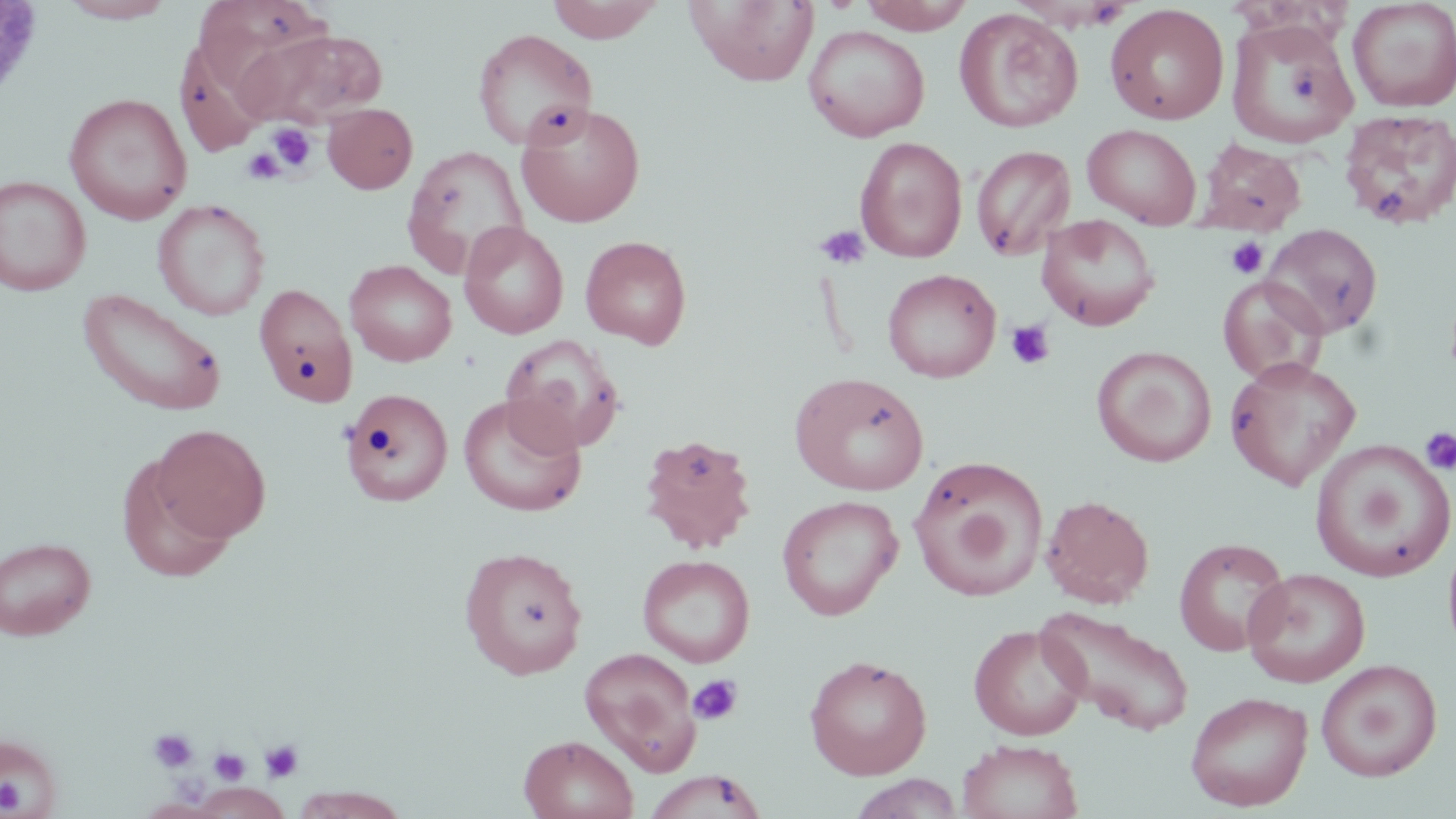

Summary:
  - Coordinate format: approximate bounding boxes as (x1,y1)-(x2,y2) corner pairs in pixels
  - Uninfected red blood cell locations: (59,0)-(176,23), (194,0)-(329,90), (546,0)-(665,43), (686,0)-(819,86), (856,0)-(976,33), (1347,0)-(1456,113), (1105,4)-(1229,125), (954,8)-(1083,133), (1226,17)-(1359,150), (803,25)-(930,142), (234,28)-(388,128), (472,29)-(597,150), (175,39)-(270,156), (64,92)-(193,225), (516,102)-(645,227), (323,103)-(418,194), (1338,108)-(1456,230), (1082,124)-(1201,227), (854,136)-(968,263), (1197,139)-(1307,233), (401,144)-(530,278), (970,144)-(1076,261), (0,175)-(92,296), (153,199)-(270,321), (1036,214)-(1160,331), (459,222)-(569,339), (1262,223)-(1383,338), (580,235)-(692,349), (345,259)-(457,367), (882,268)-(1001,382), (1218,275)-(1329,386), (253,283)-(358,407), (77,288)-(228,417), (500,334)-(625,454), (1092,346)-(1217,467), (1225,356)-(1361,490), (789,371)-(930,496), (340,387)-(455,507), (458,395)-(586,518), (152,424)-(270,543), (638,433)-(758,554), (1310,438)-(1456,582), (116,454)-(239,581), (908,455)-(1048,602), (1041,494)-(1155,608), (776,495)-(903,620), (0,536)-(96,640), (1173,537)-(1291,657), (458,545)-(588,680), (637,554)-(755,667), (1244,567)-(1371,688), (1036,606)-(1196,736), (968,624)-(1089,741), (579,646)-(702,774), (804,654)-(932,779), (1316,659)-(1443,781), (1185,690)-(1313,811), (0,731)-(64,816), (519,734)-(639,819), (957,739)-(1084,819), (642,770)-(768,819), (850,773)-(963,818), (193,783)-(290,817), (289,787)-(411,818), (139,799)-(221,818)
  - Platelet locations: (267,123)-(317,173), (242,147)-(285,185), (814,224)-(871,270), (1225,235)-(1269,279), (1006,320)-(1055,370), (1419,427)-(1456,475), (688,674)-(744,726), (148,727)-(198,773), (259,738)-(305,783), (209,747)-(250,786), (0,776)-(25,814)
  - Slide-level diagnosis: negative for blood parasites
  - Stain: May-Grünwald-Giemsa
  - Magnification: 1000x
  - Field of view: single
  - Preparation: thin blood film
  - Modality: light microscopy
  - Image size: 1456×819 pixels